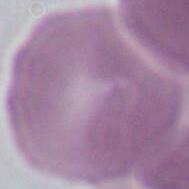

modality = micrograph
identification = Plasmodium
magnification = 400x or 1000x